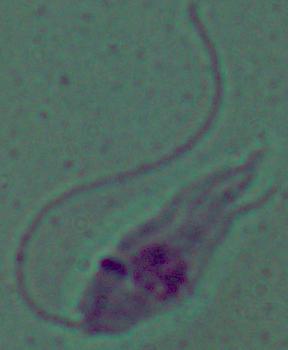
magnification = 1000x
identification = Leishmania
modality = micrograph